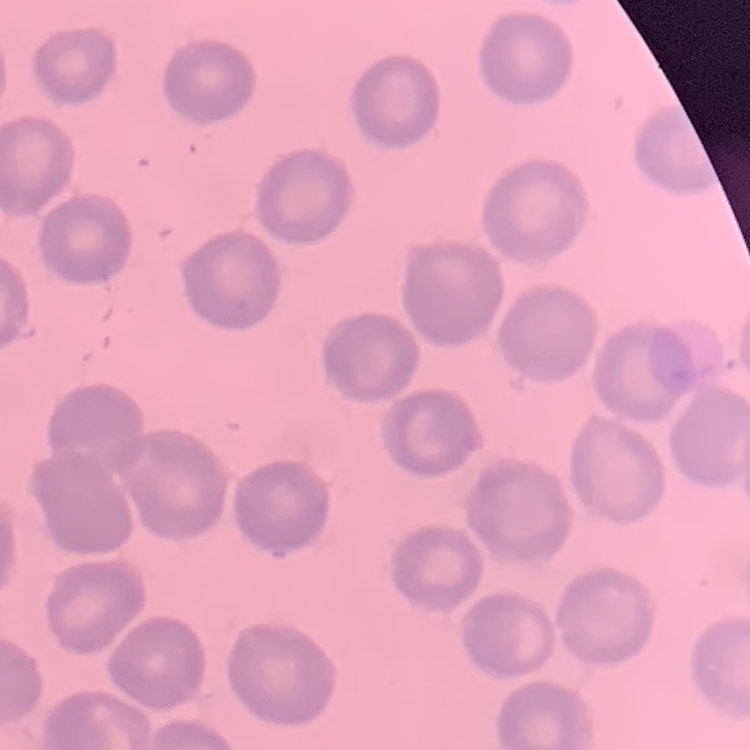 The erythrocytes show no rouleaux formation. Field's or Giemsa stain. One tile cut from a larger photomicrograph. Thin blood film.